Assess this cell for malaria.
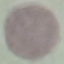

It is uninfected.

Giemsa-stained preparation. Cell patch, automatically extracted from a larger field of view and resized to 64 × 64 pixels. Acquired by smartphone through the microscope eyepiece. Thin blood film.